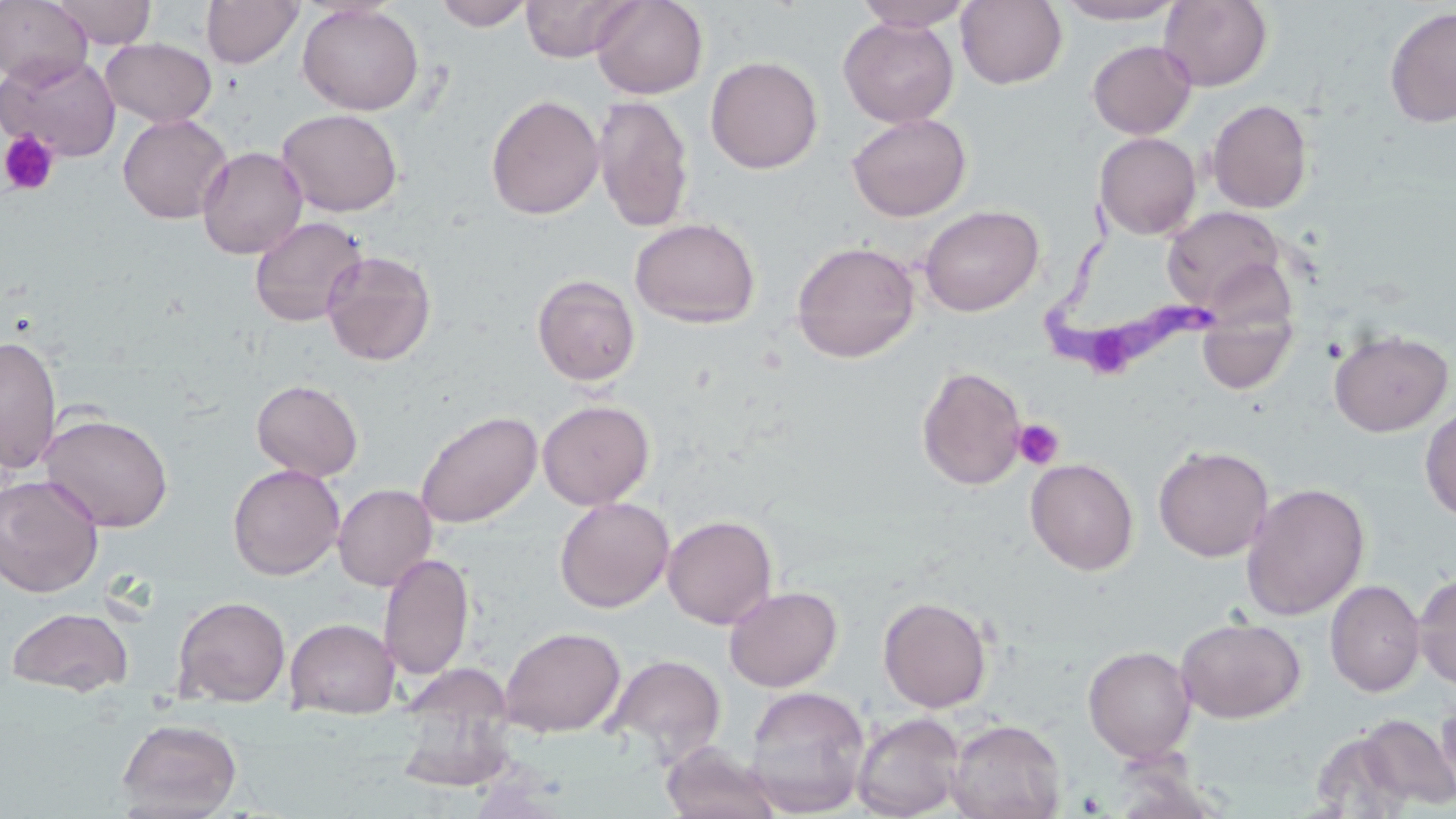
Approximate bounding boxes as named x1/y1/x2/y2 corners in pixels. Trypanosoma brucei locations: (x1=1042, y1=203, x2=1219, y2=375). Uninfected red blood cell locations: (x1=0, y1=0, x2=93, y2=87), (x1=49, y1=0, x2=156, y2=49), (x1=201, y1=0, x2=304, y2=68), (x1=433, y1=0, x2=534, y2=30), (x1=520, y1=0, x2=640, y2=62), (x1=591, y1=0, x2=707, y2=99), (x1=852, y1=0, x2=972, y2=31), (x1=1054, y1=0, x2=1187, y2=25), (x1=956, y1=1, x2=1068, y2=89), (x1=1158, y1=1, x2=1273, y2=91), (x1=297, y1=3, x2=424, y2=115), (x1=1384, y1=6, x2=1456, y2=127), (x1=838, y1=17, x2=959, y2=128), (x1=100, y1=38, x2=216, y2=127), (x1=1087, y1=40, x2=1197, y2=139), (x1=1, y1=52, x2=121, y2=161), (x1=705, y1=56, x2=823, y2=174), (x1=485, y1=94, x2=605, y2=220), (x1=592, y1=94, x2=694, y2=233), (x1=1207, y1=99, x2=1313, y2=213), (x1=277, y1=108, x2=403, y2=216), (x1=846, y1=112, x2=972, y2=222), (x1=118, y1=114, x2=232, y2=224), (x1=1094, y1=132, x2=1201, y2=240), (x1=196, y1=146, x2=308, y2=259), (x1=919, y1=204, x2=1044, y2=316), (x1=1161, y1=205, x2=1289, y2=317), (x1=249, y1=216, x2=368, y2=327), (x1=629, y1=217, x2=760, y2=328), (x1=791, y1=241, x2=920, y2=363), (x1=321, y1=250, x2=437, y2=366), (x1=532, y1=274, x2=641, y2=386), (x1=1198, y1=312, x2=1296, y2=395), (x1=1329, y1=329, x2=1453, y2=437), (x1=0, y1=335, x2=61, y2=473), (x1=917, y1=366, x2=1028, y2=491), (x1=251, y1=379, x2=363, y2=482), (x1=538, y1=400, x2=654, y2=510), (x1=1420, y1=408, x2=1456, y2=522), (x1=415, y1=409, x2=543, y2=529), (x1=40, y1=412, x2=174, y2=532), (x1=1153, y1=445, x2=1274, y2=562), (x1=1025, y1=458, x2=1139, y2=575), (x1=227, y1=463, x2=345, y2=580), (x1=0, y1=474, x2=103, y2=598), (x1=1240, y1=482, x2=1370, y2=621), (x1=333, y1=483, x2=437, y2=591), (x1=554, y1=496, x2=675, y2=613), (x1=663, y1=515, x2=778, y2=629), (x1=378, y1=552, x2=475, y2=682), (x1=1413, y1=571, x2=1456, y2=692), (x1=1325, y1=579, x2=1425, y2=697), (x1=723, y1=585, x2=842, y2=692), (x1=172, y1=595, x2=291, y2=707), (x1=878, y1=595, x2=992, y2=713), (x1=5, y1=606, x2=134, y2=697), (x1=1175, y1=616, x2=1305, y2=723), (x1=284, y1=617, x2=401, y2=719), (x1=499, y1=626, x2=625, y2=736), (x1=1083, y1=645, x2=1197, y2=762), (x1=603, y1=654, x2=726, y2=766), (x1=391, y1=666, x2=519, y2=794), (x1=743, y1=685, x2=871, y2=817), (x1=1436, y1=694, x2=1456, y2=800), (x1=851, y1=711, x2=966, y2=819), (x1=1352, y1=714, x2=1456, y2=812), (x1=116, y1=717, x2=242, y2=817), (x1=946, y1=718, x2=1066, y2=819), (x1=1309, y1=725, x2=1418, y2=816), (x1=661, y1=743, x2=782, y2=819). Platelet locations: (x1=0, y1=131, x2=60, y2=196), (x1=1012, y1=419, x2=1064, y2=470). Slide-level diagnosis: Trypanosoma brucei. One field of a larger specimen. Image is 1456×819 pixels. Thin blood film. Captured at 1000x magnification. May-Grünwald-Giemsa-stained preparation. Optical microscopy.